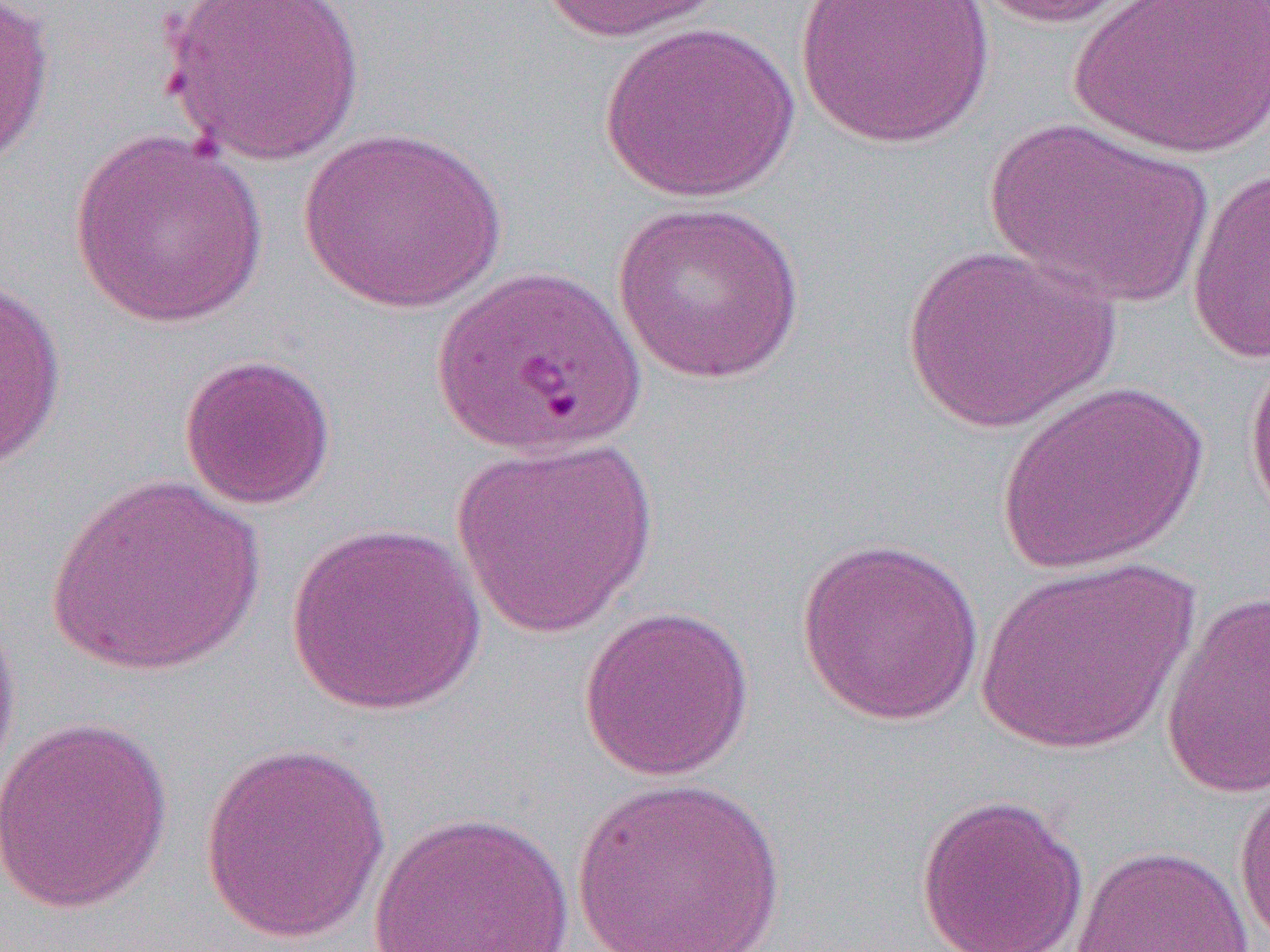

Summary:
  - Coordinate format: approximate bounding boxes as (x1,y1)-(x2,y2) corner pairs in pixels
  - Uninfected red blood cell locations: (0,0)-(57,171), (159,0)-(367,169), (534,0)-(731,43), (796,0)-(995,149), (964,0)-(1151,30), (1070,0)-(1269,160), (600,21)-(802,202), (981,116)-(1215,309), (297,126)-(509,313), (69,129)-(269,329), (1185,166)-(1270,365), (611,200)-(806,385), (900,244)-(1120,433), (0,276)-(67,474), (1244,339)-(1270,536), (178,353)-(337,511), (994,378)-(1210,576), (451,437)-(659,639), (45,471)-(265,678), (286,521)-(488,715), (794,535)-(987,727), (976,557)-(1198,756), (1160,589)-(1270,800), (578,604)-(756,782), (0,605)-(22,802), (0,714)-(173,915), (198,740)-(391,944), (1232,765)-(1270,949), (570,775)-(787,951), (915,792)-(1089,952), (368,810)-(575,952), (1069,843)-(1256,951)
  - Slide-level diagnosis: Plasmodium falciparum
  - Modality: optical microscopy
  - Preparation: thin blood film
  - Field of view: one of a larger specimen
  - Magnification: 1000x
  - Image size: 1270×952 pixels